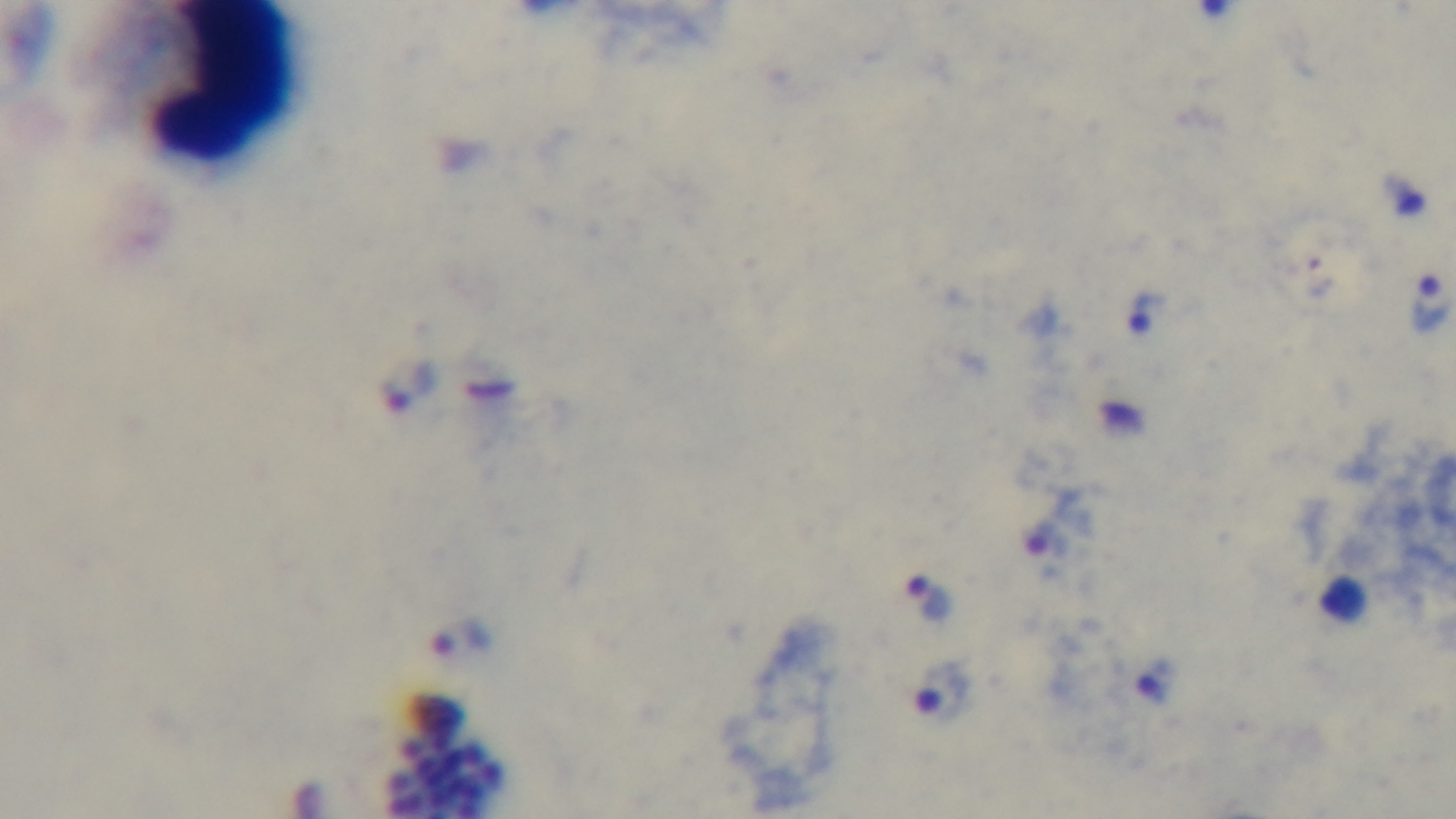

Photomicrograph. Single field of view. Oil-immersion objective, 100x. Malaria status: positive. Captured with a mounted 4K digital camera. Preparation: thick smear. Giemsa-stained.